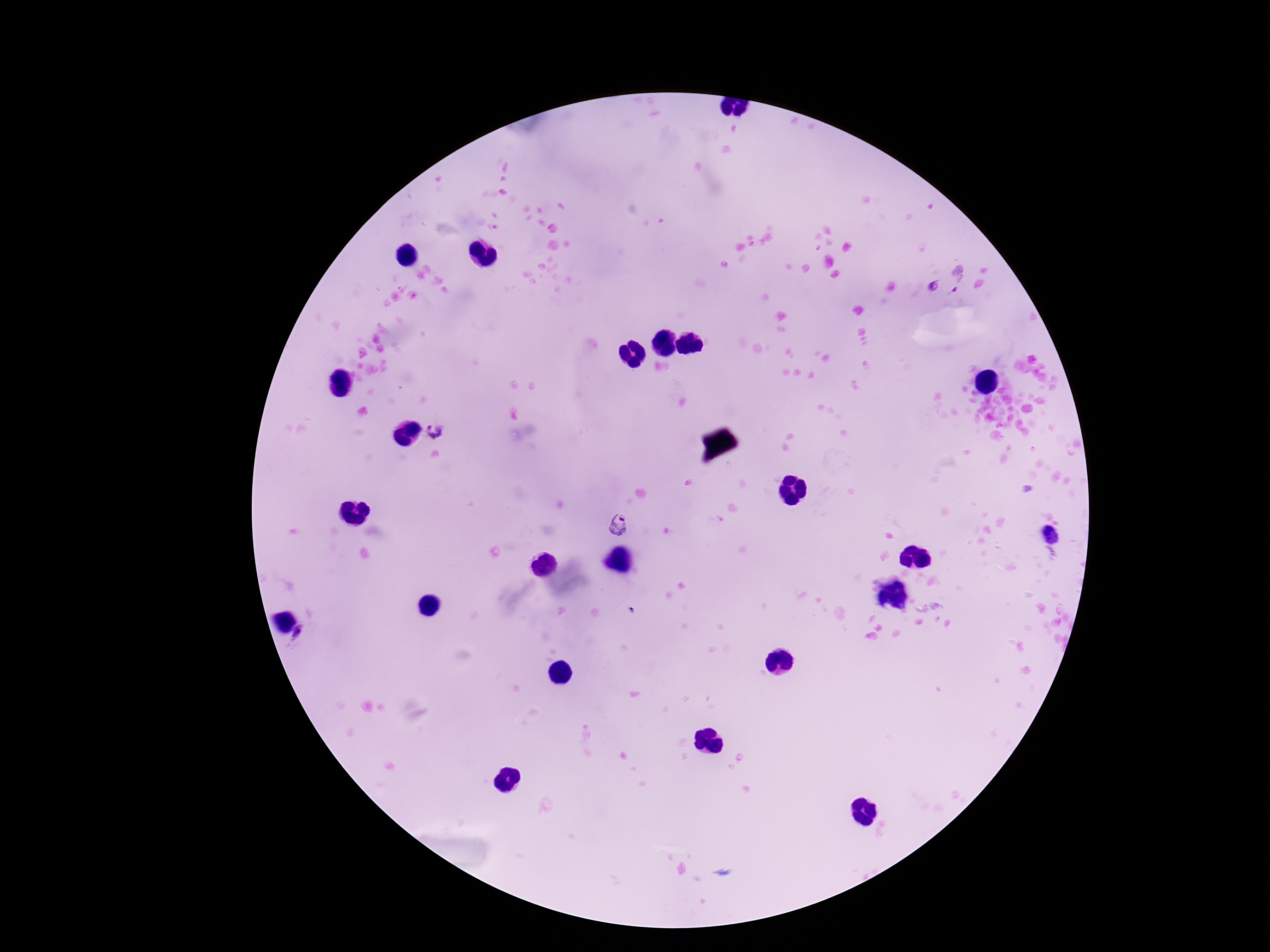
image_size: 1270×952 pixels
patient_malaria_status: positive
stain: Giemsa
capture: smartphone camera through the microscope eyepiece
magnification: 100x
plasmodium_parasite_locations: 'approximate object centers, in pixels from the top-left corner: (x=958, y=277), (x=933, y=285), (x=436, y=433), (x=621, y=527)'
preparation: thick peripheral-blood smear
field_of_view: one from this slide